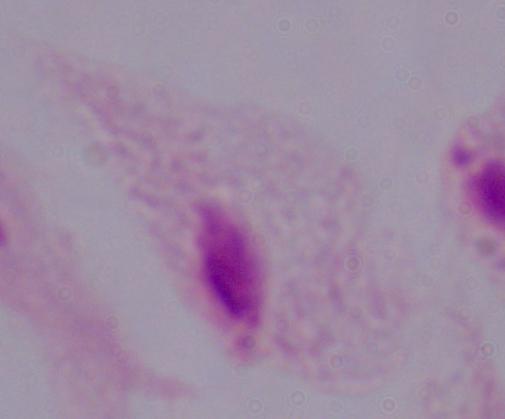

Summary:
  - Modality: photomicrograph
  - Magnification: 1000x
  - Identification: trichomonad